Locate every blood parasite and identify its species.
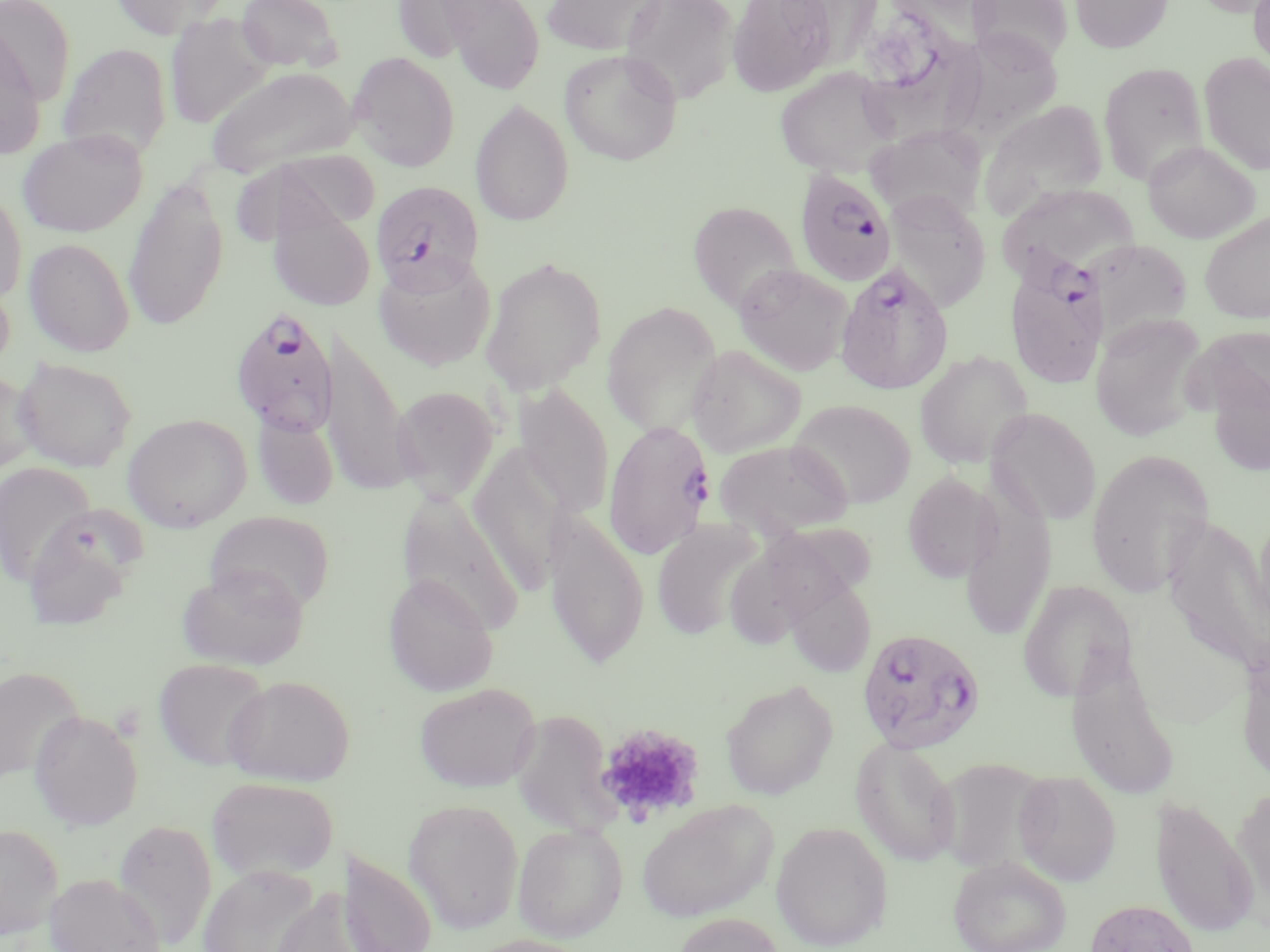

Approximate bounding boxes as [x1, y1, x2, y2] in pixels.
Plasmodium falciparum-infected red blood cells: [793, 168, 898, 289], [371, 180, 483, 293], [1005, 255, 1108, 388], [834, 262, 954, 395], [229, 308, 339, 436], [602, 420, 716, 560], [856, 628, 986, 754].
No Plasmodium ovale, Plasmodium malariae, Plasmodium vivax, Babesia divergens, or Trypanosoma brucei observed.

Summary:
  - Platelet locations: [595, 722, 705, 823]
  - Uninfected red blood cell locations: [0, 0, 76, 106], [110, 0, 230, 40], [235, 0, 343, 73], [540, 0, 667, 56], [618, 0, 740, 106], [727, 0, 837, 97], [967, 0, 1073, 67], [1070, 0, 1173, 53], [1190, 0, 1270, 17], [1249, 0, 1270, 74], [390, 1, 504, 64], [437, 1, 546, 92], [166, 12, 273, 130], [0, 20, 46, 160], [860, 36, 983, 146], [57, 42, 172, 162], [559, 48, 683, 166], [1199, 51, 1270, 176], [348, 52, 460, 172], [1099, 63, 1208, 186], [205, 65, 359, 178], [774, 66, 899, 178], [471, 99, 574, 226], [980, 100, 1109, 220], [866, 124, 988, 225], [18, 129, 147, 238], [221, 138, 380, 245], [1143, 140, 1260, 243], [123, 177, 229, 331], [998, 181, 1140, 278], [0, 187, 27, 307], [884, 190, 991, 312], [688, 200, 801, 314], [269, 201, 376, 312], [1199, 211, 1270, 324], [23, 238, 135, 357], [1092, 238, 1192, 345], [373, 252, 497, 371], [480, 256, 607, 395], [733, 263, 853, 376], [601, 300, 723, 436], [1090, 313, 1209, 442], [319, 323, 413, 496], [686, 344, 806, 457], [914, 350, 1034, 470], [13, 357, 137, 472], [0, 369, 38, 477], [514, 384, 614, 518], [391, 386, 500, 502], [788, 399, 916, 508], [986, 407, 1101, 526], [253, 410, 338, 511], [122, 413, 252, 532], [714, 438, 852, 538], [468, 445, 572, 594], [1086, 449, 1215, 596], [0, 461, 98, 585], [903, 472, 994, 583], [397, 490, 525, 632], [960, 490, 1057, 641], [1253, 506, 1270, 636], [544, 507, 649, 669], [21, 509, 143, 631], [205, 511, 334, 615], [652, 520, 763, 640], [729, 524, 881, 646], [176, 564, 309, 670], [383, 573, 498, 696], [783, 575, 877, 678], [1017, 580, 1135, 702], [1235, 635, 1270, 788], [153, 658, 271, 770], [0, 664, 84, 783], [224, 674, 354, 786], [720, 680, 838, 800], [413, 682, 541, 792], [512, 704, 624, 850], [29, 710, 143, 830], [850, 736, 962, 867], [934, 756, 1051, 875], [1013, 769, 1122, 886], [206, 776, 340, 883], [1232, 784, 1270, 916], [1149, 796, 1258, 940], [403, 798, 524, 933], [636, 799, 778, 922], [112, 819, 216, 949], [770, 820, 893, 951], [512, 822, 627, 942], [0, 824, 64, 940], [338, 850, 437, 952], [948, 854, 1072, 952], [197, 864, 324, 952], [44, 873, 167, 952], [269, 887, 385, 952], [1084, 897, 1202, 952], [670, 913, 787, 952], [463, 934, 596, 952]
  - Slide-level diagnosis: Plasmodium falciparum
  - Modality: light microscopy
  - Preparation: thin blood smear
  - Stain: May-Grünwald-Giemsa
  - Field of view: one of a larger specimen
  - Image size: 1270×952 pixels
  - Magnification: 1000x